Report the malaria status of this cell.
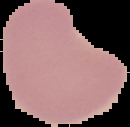

Uninfected.

Summary:
  - Image size: 130×127 pixels
  - Preparation: thin blood film
  - Image type: cell region segmented out of the field of view; surrounding area masked to black